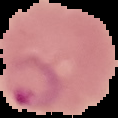
Summary:
  - Malaria status: parasitized
  - Image type: segmented cell region with the area outside set to black
  - Preparation: thin blood smear
  - Image size: 118×118 pixels